Classify this cell by malaria status.
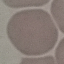

It is uninfected.

{
  "stain": "Giemsa",
  "preparation": "thin blood smear",
  "capture": "smartphone through the microscope eyepiece",
  "image_type": "cell patch, automatically extracted from a larger field of view and resized to 64 × 64 pixels"
}